Classify this cell by malaria status.
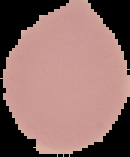

Uninfected.

From a thin blood film. Image is 130×157 pixels. The area outside the segmented cell region is set to black.